Assess the morphology of the erythrocytes.
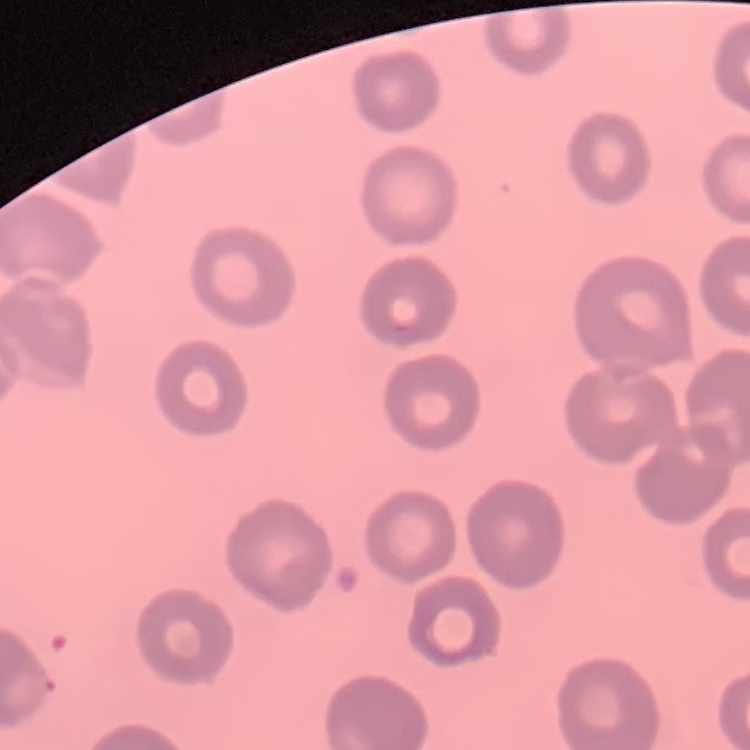

No rouleaux formation.

Stained with either Field's or Giemsa. Thin blood film. One tile cut from a larger photomicrograph.